Give the extent of all white blood cells.
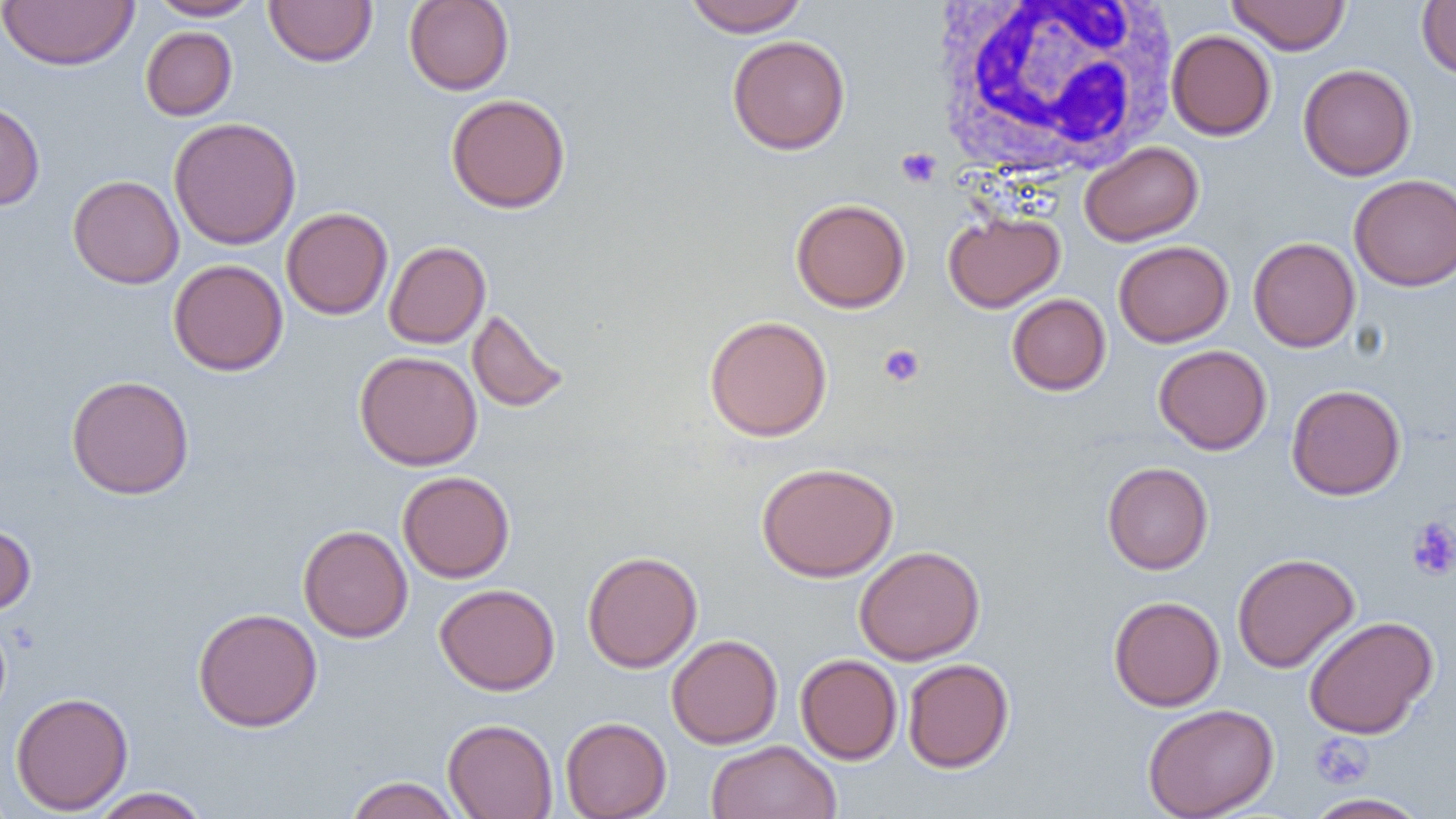

Approximate bounding boxes as [x1, y1, x2, y2] in pixels.
White blood cells: [928, 0, 1181, 181].

Summary:
  - Platelet locations: [896, 147, 941, 188], [878, 344, 925, 387], [1406, 517, 1456, 582], [1309, 733, 1374, 790]
  - Uninfected red blood cell locations: [1, 0, 139, 70], [148, 0, 262, 21], [264, 0, 377, 67], [684, 0, 808, 36], [1227, 0, 1350, 55], [404, 1, 514, 95], [1416, 1, 1456, 79], [140, 27, 237, 120], [1167, 30, 1276, 140], [727, 34, 851, 155], [1298, 63, 1416, 181], [446, 93, 571, 213], [0, 100, 45, 210], [168, 116, 302, 250], [1079, 141, 1204, 246], [1349, 173, 1456, 291], [68, 174, 184, 289], [790, 198, 911, 313], [281, 207, 393, 320], [944, 211, 1065, 312], [1248, 237, 1360, 352], [384, 240, 491, 349], [1113, 240, 1233, 347], [168, 259, 288, 376], [1007, 293, 1111, 396], [467, 308, 570, 414], [704, 314, 833, 442], [1153, 344, 1272, 455], [355, 350, 483, 470], [66, 374, 195, 500], [1286, 384, 1406, 500], [757, 461, 898, 582], [1102, 461, 1214, 574], [398, 470, 515, 583], [0, 522, 36, 615], [298, 524, 413, 642], [854, 545, 985, 665], [582, 550, 702, 673], [1232, 552, 1360, 673], [434, 583, 560, 696], [1108, 595, 1225, 711], [193, 607, 323, 732], [1303, 616, 1439, 739], [666, 634, 783, 749], [795, 654, 902, 765], [902, 658, 1014, 773], [11, 692, 133, 815], [1142, 703, 1279, 819], [560, 716, 672, 819], [443, 718, 558, 819], [705, 740, 841, 819], [345, 775, 464, 819], [88, 787, 210, 819], [1303, 792, 1432, 819]
  - Slide-level diagnosis: negative for blood parasites
  - Preparation: thin blood film
  - Field of view: single
  - Image size: 1456×819 pixels
  - Modality: optical microscopy
  - Magnification: 1000x